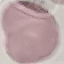 Malaria status: uninfected. Thin smear of blood. Photographed with a smartphone camera at the microscope eyepiece. Automatically extracted cell patch, resized to 64 × 64 pixels. Giemsa-stained preparation.